Classify this cell by malaria status.
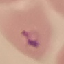
It is parasitized.

Cell patch, automatically extracted from a larger field of view and resized to 64 × 64 pixels. Thin smear of blood. Giemsa-stained preparation. Acquired by smartphone through the microscope eyepiece.